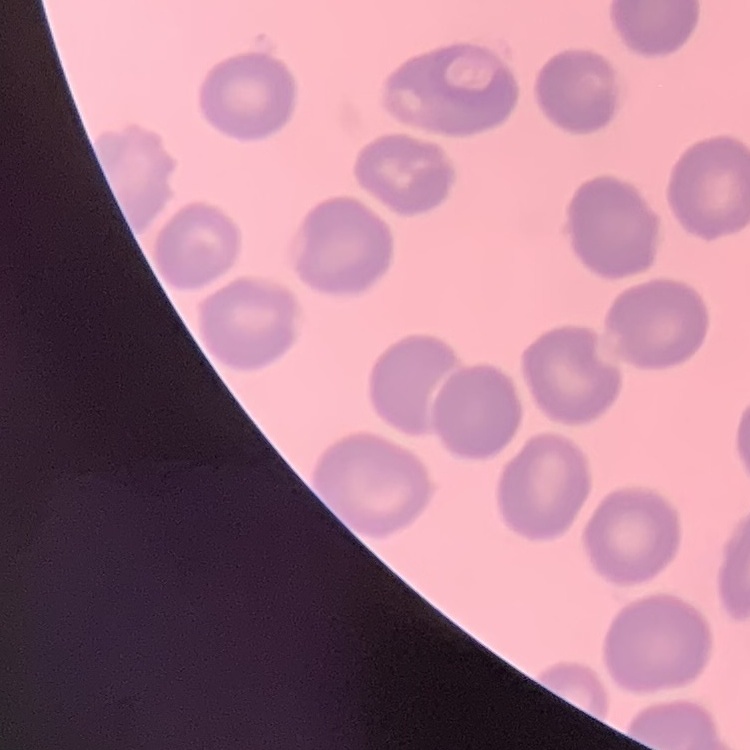

The red blood cells show no rouleaux formation. Square crop of a larger photomicrograph. Field's or Giemsa stain. Thin blood smear.